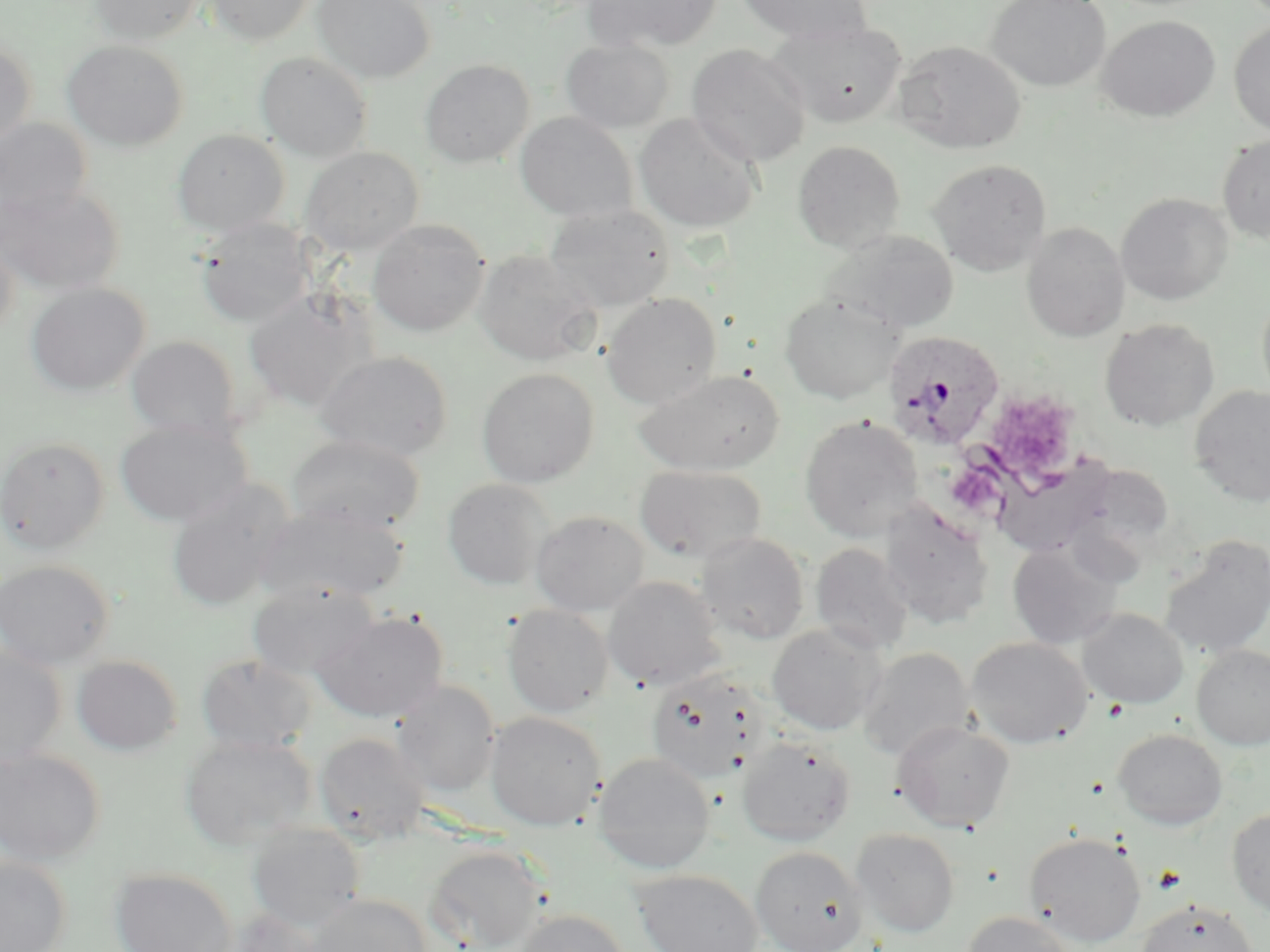

Summary:
  - Coordinate format: approximate bounding boxes as [x1, y1, x2, y2] in pixels
  - Uninfected red blood cell locations: [89, 0, 204, 44], [206, 0, 319, 45], [313, 0, 435, 83], [584, 0, 721, 53], [735, 0, 873, 44], [986, 0, 1111, 92], [1098, 15, 1220, 122], [774, 20, 907, 128], [1229, 21, 1270, 137], [561, 38, 674, 133], [0, 39, 37, 147], [62, 39, 189, 151], [893, 40, 1026, 154], [687, 44, 811, 168], [255, 51, 373, 162], [420, 58, 534, 168], [515, 112, 638, 222], [634, 113, 762, 233], [0, 118, 92, 221], [172, 128, 289, 235], [1217, 135, 1270, 243], [792, 140, 906, 253], [300, 146, 423, 254], [928, 158, 1052, 276], [0, 184, 125, 296], [1116, 193, 1233, 305], [545, 204, 676, 311], [195, 218, 313, 328], [368, 219, 490, 336], [1021, 223, 1129, 342], [823, 230, 959, 333], [0, 235, 19, 339], [473, 249, 600, 366], [26, 282, 150, 397], [243, 291, 373, 412], [1256, 292, 1270, 407], [601, 293, 722, 409], [779, 293, 904, 404], [1099, 318, 1219, 431], [126, 335, 242, 440], [317, 350, 452, 461], [477, 367, 599, 487], [634, 369, 784, 475], [1189, 385, 1270, 506], [799, 415, 924, 541], [114, 418, 252, 527], [287, 435, 426, 535], [0, 436, 110, 553], [993, 455, 1120, 559], [634, 465, 767, 564], [442, 478, 553, 590], [166, 480, 292, 612], [879, 501, 994, 630], [258, 503, 408, 604], [530, 510, 650, 616], [696, 532, 809, 644], [1160, 535, 1270, 660], [1008, 540, 1123, 649], [810, 542, 914, 655], [0, 559, 115, 669], [602, 576, 725, 691], [248, 581, 378, 680], [503, 603, 613, 717], [1077, 608, 1188, 708], [314, 610, 449, 723], [766, 623, 886, 736], [966, 636, 1093, 748], [1191, 643, 1270, 749], [0, 645, 66, 768], [857, 647, 974, 761], [72, 654, 183, 756], [197, 654, 317, 755], [645, 670, 767, 784], [393, 681, 500, 796], [485, 711, 605, 830], [892, 720, 1015, 833], [1113, 727, 1228, 830], [314, 731, 430, 844], [180, 733, 317, 849], [738, 735, 856, 847], [0, 747, 106, 866], [593, 752, 716, 874], [1227, 807, 1270, 914], [248, 824, 365, 930], [850, 827, 960, 938], [1024, 831, 1146, 947], [425, 844, 549, 952], [750, 845, 869, 952], [0, 856, 71, 952], [109, 867, 238, 952], [631, 869, 763, 952], [306, 894, 432, 952], [1135, 899, 1259, 952], [221, 908, 324, 952], [512, 908, 631, 952], [961, 911, 1079, 952]
  - Plasmodium ovale-infected red blood cell locations: [882, 329, 1006, 451]
  - Platelet locations: [1153, 865, 1187, 893]
  - Slide-level diagnosis: Plasmodium ovale
  - Field of view: one of a larger specimen
  - Modality: optical microscopy
  - Magnification: 1000x
  - Stain: May-Grünwald-Giemsa
  - Preparation: thin blood smear
  - Image size: 1270×952 pixels